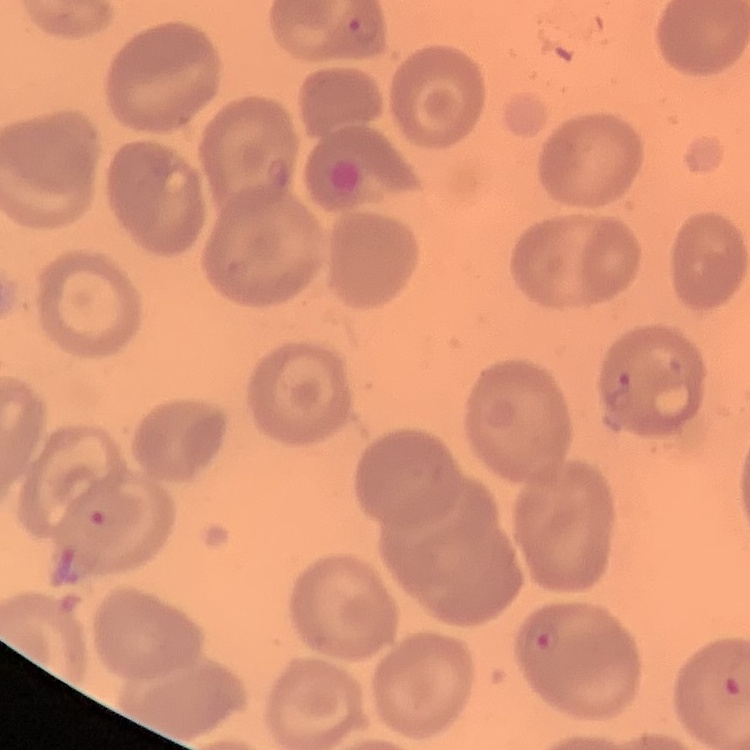
The red blood cells exhibit no rouleaux formation. Thin blood smear. Stained with either Field's or Giemsa. One tile cut from a larger photomicrograph.